Report the malaria status of this cell.
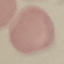
Uninfected.

{
  "image_type": "cell patch, automatically extracted from a larger field of view and resized to 64 × 64 pixels",
  "stain": "Giemsa",
  "preparation": "thin blood smear",
  "capture": "smartphone camera at the microscope eyepiece"
}